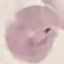

result = malaria parasites detected
preparation = thin blood film
stain = Giemsa
image type = cell patch, automatically extracted from a larger field of view and resized to 64 × 64 pixels
capture = smartphone through the microscope eyepiece